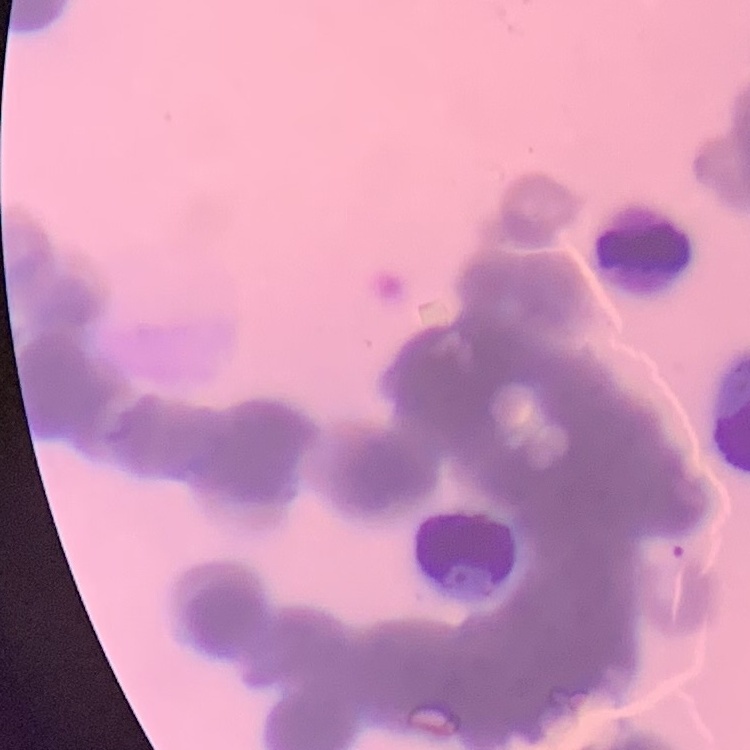
{
  "erythrocyte_morphology": "rouleaux formation",
  "preparation": "thin blood film",
  "image_type": "square crop of a larger photomicrograph",
  "stain": "Field's or Giemsa"
}